Classify this cell by malaria status.
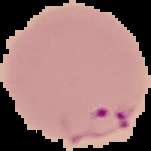
Parasitized.

Summary:
  - Image size: 151×151 pixels
  - Preparation: thin blood film
  - Image type: cell region segmented out of the field of view; surrounding area masked to black